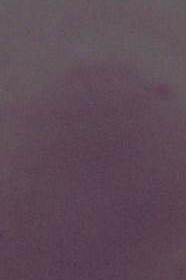

Summary:
  - Magnification: 1000x
  - Identification: erythrocyte
  - Modality: micrograph